Describe the morphology of the red blood cells.
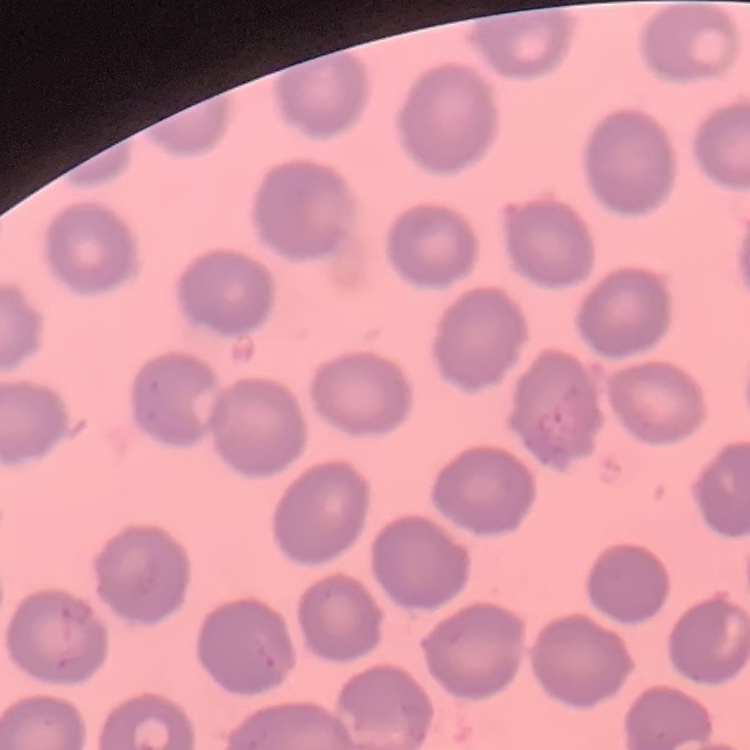

No rouleaux formation.

Stained with either Field's or Giemsa. Square crop of a larger photomicrograph. Thin peripheral smear.